Outline each Plasmodium malariae-infected red blood cell.
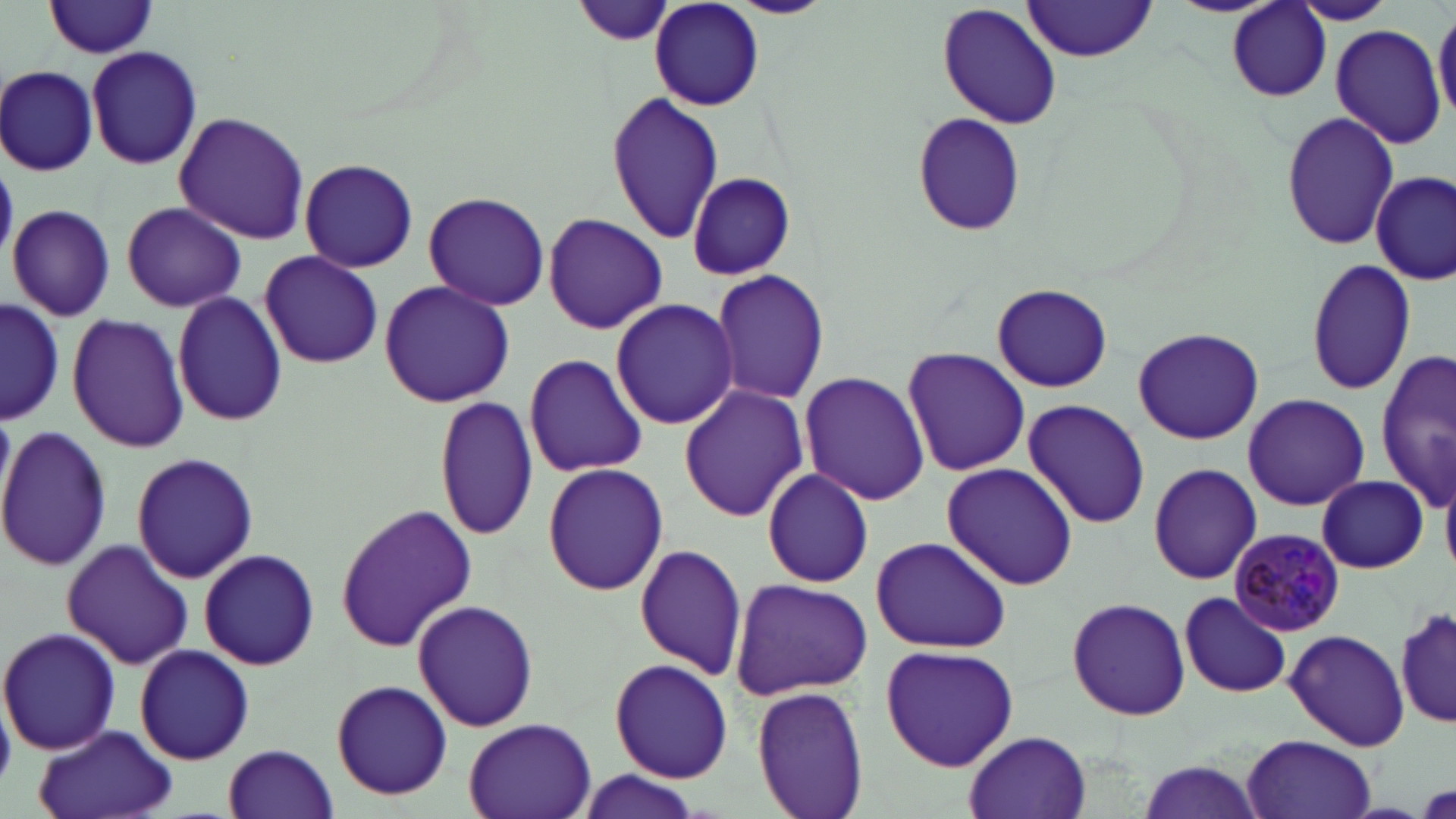

Approximate bounding boxes as [x1, y1, x2, y2] in pixels.
Plasmodium malariae-infected red blood cells: [1231, 526, 1345, 638].

{
  "slide_level_diagnosis": "Plasmodium malariae",
  "image_size": "1456×819 pixels",
  "uninfected_red_blood_cell_locations": "approximate bounding boxes as [x1, y1, x2, y2] in pixels: [572, 0, 676, 49], [725, 0, 835, 19], [1169, 0, 1277, 17], [1287, 0, 1398, 25], [43, 1, 160, 58], [650, 1, 765, 110], [1020, 1, 1160, 63], [1227, 2, 1333, 102], [937, 3, 1064, 131], [1433, 9, 1455, 123], [1330, 25, 1447, 149], [86, 45, 203, 171], [1, 65, 99, 176], [603, 91, 723, 245], [1279, 108, 1394, 252], [174, 111, 310, 245], [909, 111, 1029, 237], [297, 157, 420, 273], [1373, 171, 1453, 284], [686, 172, 796, 279], [422, 191, 552, 310], [121, 202, 244, 313], [7, 203, 115, 322], [543, 213, 669, 333], [260, 249, 383, 370], [1304, 259, 1417, 397], [710, 271, 832, 405], [378, 281, 515, 408], [990, 283, 1115, 392], [171, 291, 289, 428], [2, 298, 64, 426], [610, 298, 739, 432], [65, 312, 189, 454], [1133, 325, 1265, 445], [901, 347, 1029, 476], [522, 352, 650, 477], [1375, 352, 1455, 505], [798, 370, 930, 505], [679, 384, 809, 522], [1242, 393, 1370, 511], [433, 395, 540, 543], [1022, 398, 1151, 529], [0, 423, 111, 574], [130, 452, 259, 582], [1146, 461, 1263, 586], [543, 462, 668, 596], [942, 462, 1078, 590], [760, 469, 878, 589], [1316, 475, 1428, 574], [334, 503, 478, 653], [867, 536, 1011, 653], [61, 538, 192, 671], [634, 541, 749, 682], [199, 548, 320, 670], [730, 576, 874, 699], [1180, 591, 1292, 698], [1066, 597, 1191, 721], [411, 599, 538, 731], [1399, 603, 1455, 733], [0, 626, 120, 756], [1284, 629, 1410, 753], [134, 644, 254, 764], [881, 644, 1020, 772], [609, 658, 733, 783], [330, 679, 453, 802], [751, 684, 871, 819], [463, 716, 598, 819], [29, 723, 175, 819], [962, 731, 1092, 818], [1242, 735, 1378, 819], [223, 744, 339, 819], [1133, 756, 1268, 819], [565, 773, 709, 817]",
  "modality": "light microscopy",
  "magnification": "1000x",
  "field_of_view": "single",
  "preparation": "thin blood smear",
  "stain": "May-Grünwald-Giemsa"
}